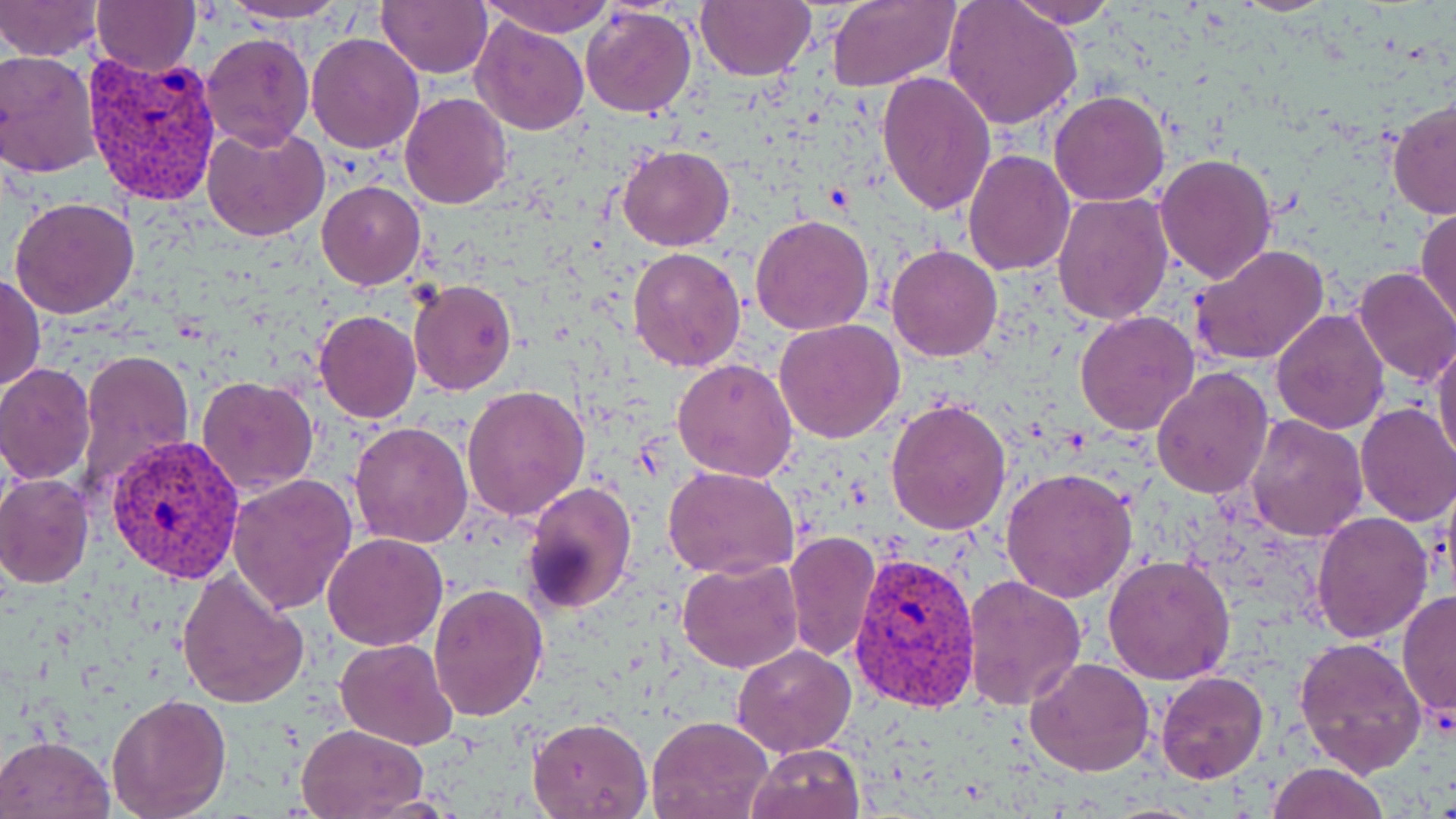

Approximate bounding boxes as [x1, y1, x2, y2] in pixels. Uninfected red blood cell locations: [0, 0, 103, 61], [223, 0, 352, 25], [377, 0, 492, 78], [480, 0, 617, 38], [696, 0, 814, 81], [826, 0, 960, 90], [1006, 0, 1121, 28], [1233, 0, 1337, 15], [941, 1, 1082, 131], [92, 2, 200, 76], [581, 6, 697, 119], [471, 14, 592, 135], [201, 31, 315, 152], [306, 31, 424, 153], [0, 51, 102, 178], [875, 70, 995, 216], [1048, 91, 1171, 207], [399, 93, 514, 210], [1386, 99, 1456, 220], [202, 123, 329, 241], [617, 144, 736, 251], [963, 149, 1075, 276], [1153, 153, 1279, 285], [317, 181, 426, 290], [1052, 190, 1175, 325], [9, 196, 140, 320], [1416, 205, 1456, 329], [751, 213, 875, 336], [886, 244, 1003, 362], [1189, 244, 1332, 368], [629, 246, 745, 372], [1350, 265, 1456, 388], [2, 272, 45, 393], [409, 280, 517, 397], [1270, 310, 1390, 434], [314, 311, 422, 423], [1074, 311, 1200, 436], [775, 319, 905, 444], [1432, 334, 1456, 469], [75, 349, 195, 492], [673, 359, 799, 482], [0, 363, 96, 484], [1151, 368, 1273, 501], [197, 375, 318, 496], [463, 384, 588, 521], [886, 397, 1012, 535], [1354, 401, 1456, 526], [1243, 413, 1367, 541], [349, 422, 474, 548], [664, 465, 800, 579], [1002, 466, 1136, 603], [0, 474, 94, 588], [228, 475, 359, 616], [520, 480, 637, 617], [1312, 513, 1433, 643], [783, 531, 880, 662], [321, 532, 448, 650], [1104, 554, 1237, 685], [677, 558, 804, 674], [175, 569, 309, 709], [962, 574, 1087, 710], [427, 583, 548, 722], [1396, 590, 1456, 726], [1295, 636, 1426, 778], [336, 638, 457, 751], [732, 644, 856, 756], [1024, 656, 1155, 776], [1155, 670, 1269, 783], [105, 693, 232, 818], [528, 714, 653, 818], [647, 715, 772, 819], [296, 723, 428, 819], [0, 733, 115, 818], [748, 743, 865, 819], [1266, 762, 1389, 819], [356, 793, 465, 816]. Plasmodium vivax-infected red blood cell locations: [81, 51, 222, 208], [106, 432, 246, 586], [849, 551, 983, 719]. Slide-level diagnosis: Plasmodium vivax. 1000x magnification. Image is 1456×819 pixels. May-Grünwald-Giemsa-stained preparation. Thin blood film. Single field of view. Optical microscopy.